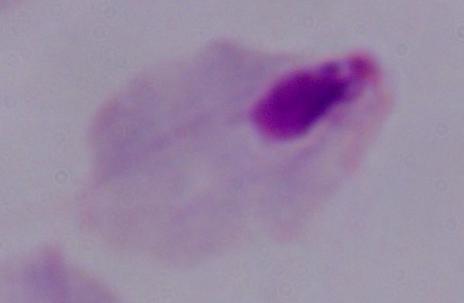
magnification = 1000x
modality = photomicrograph
identification = trichomonad